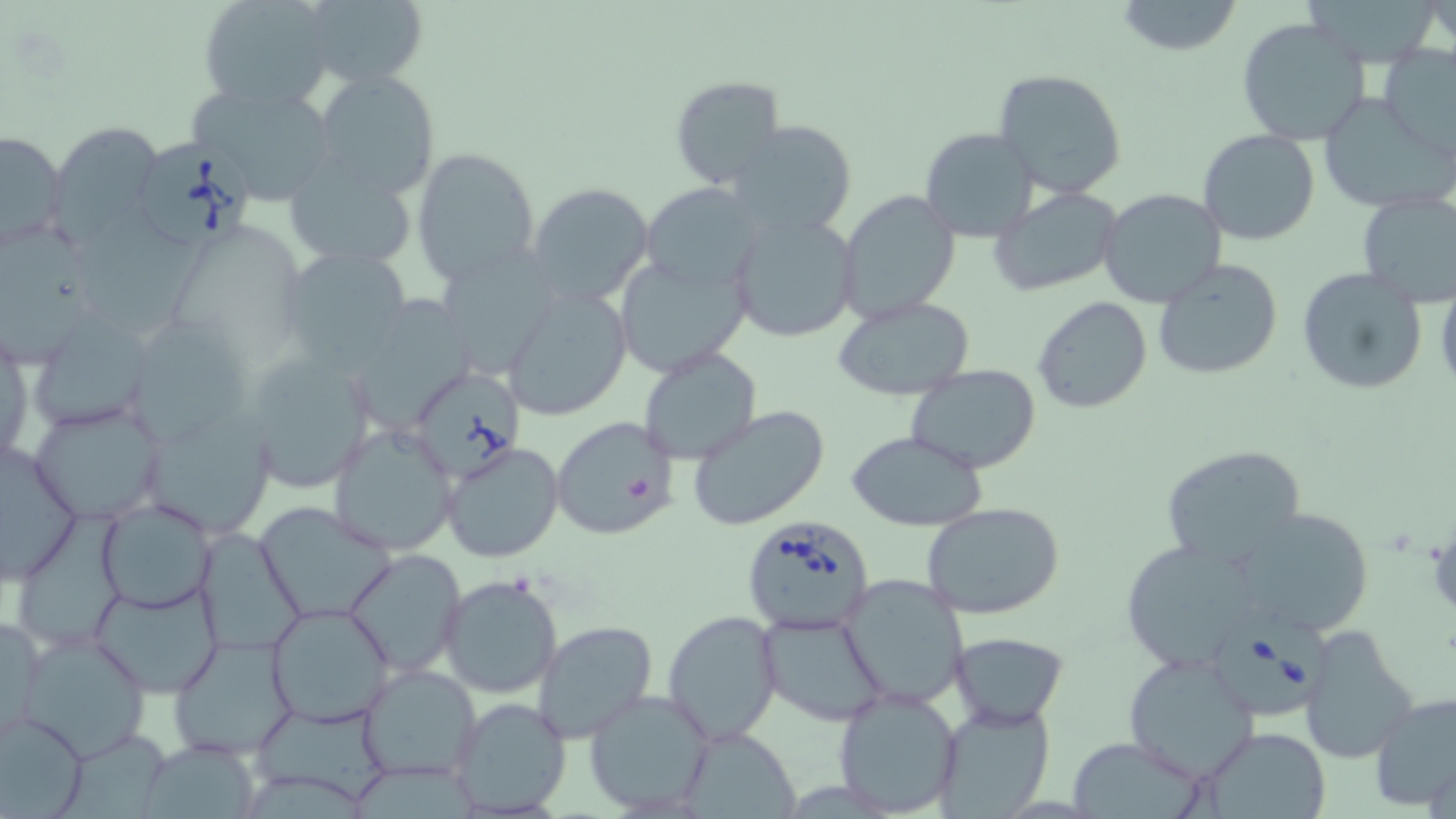
Summary:
  - Coordinate format: approximate bounding boxes as named x1/y1/x2/y2 corners in pixels
  - Uninfected red blood cell locations: (x1=199, y1=0, x2=339, y2=115), (x1=289, y1=0, x2=430, y2=94), (x1=1115, y1=0, x2=1244, y2=57), (x1=1306, y1=1, x2=1440, y2=67), (x1=1236, y1=17, x2=1371, y2=146), (x1=1377, y1=46, x2=1456, y2=157), (x1=992, y1=67, x2=1129, y2=199), (x1=312, y1=69, x2=442, y2=199), (x1=667, y1=75, x2=788, y2=192), (x1=186, y1=79, x2=341, y2=207), (x1=1317, y1=95, x2=1447, y2=214), (x1=726, y1=120, x2=859, y2=237), (x1=49, y1=123, x2=165, y2=244), (x1=919, y1=126, x2=1039, y2=244), (x1=1196, y1=128, x2=1323, y2=246), (x1=0, y1=129, x2=68, y2=250), (x1=411, y1=146, x2=542, y2=287), (x1=282, y1=158, x2=421, y2=269), (x1=528, y1=182, x2=653, y2=307), (x1=640, y1=182, x2=764, y2=294), (x1=990, y1=185, x2=1123, y2=295), (x1=1097, y1=188, x2=1226, y2=307), (x1=836, y1=190, x2=959, y2=322), (x1=1354, y1=191, x2=1456, y2=305), (x1=79, y1=206, x2=209, y2=332), (x1=728, y1=211, x2=860, y2=344), (x1=171, y1=225, x2=294, y2=362), (x1=0, y1=227, x2=108, y2=366), (x1=278, y1=245, x2=415, y2=372), (x1=437, y1=248, x2=562, y2=378), (x1=613, y1=254, x2=750, y2=377), (x1=1154, y1=259, x2=1284, y2=381), (x1=1297, y1=266, x2=1427, y2=396), (x1=502, y1=285, x2=633, y2=420), (x1=361, y1=291, x2=471, y2=431), (x1=833, y1=295, x2=975, y2=400), (x1=1031, y1=295, x2=1153, y2=415), (x1=136, y1=321, x2=251, y2=443), (x1=36, y1=322, x2=146, y2=425), (x1=1, y1=330, x2=32, y2=470), (x1=637, y1=345, x2=763, y2=464), (x1=242, y1=348, x2=379, y2=495), (x1=906, y1=363, x2=1042, y2=474), (x1=28, y1=396, x2=169, y2=525), (x1=685, y1=404, x2=831, y2=532), (x1=550, y1=416, x2=679, y2=540), (x1=146, y1=422, x2=274, y2=535), (x1=328, y1=425, x2=458, y2=556), (x1=846, y1=431, x2=991, y2=530), (x1=0, y1=436, x2=86, y2=587), (x1=440, y1=442, x2=566, y2=565), (x1=1159, y1=443, x2=1307, y2=570), (x1=96, y1=499, x2=216, y2=613), (x1=255, y1=502, x2=397, y2=623), (x1=920, y1=502, x2=1069, y2=621), (x1=1234, y1=505, x2=1375, y2=635), (x1=20, y1=508, x2=126, y2=641), (x1=194, y1=527, x2=304, y2=658), (x1=1116, y1=538, x2=1268, y2=673), (x1=344, y1=549, x2=466, y2=677), (x1=439, y1=575, x2=563, y2=699), (x1=837, y1=575, x2=970, y2=710), (x1=89, y1=578, x2=225, y2=698), (x1=264, y1=603, x2=395, y2=728), (x1=662, y1=610, x2=782, y2=743), (x1=1, y1=611, x2=45, y2=741), (x1=758, y1=612, x2=889, y2=727), (x1=532, y1=620, x2=658, y2=744), (x1=1296, y1=623, x2=1421, y2=763), (x1=14, y1=628, x2=154, y2=761), (x1=950, y1=631, x2=1068, y2=726), (x1=168, y1=634, x2=300, y2=761), (x1=1122, y1=650, x2=1259, y2=782), (x1=356, y1=664, x2=481, y2=783), (x1=830, y1=687, x2=964, y2=816), (x1=583, y1=689, x2=716, y2=817), (x1=1370, y1=692, x2=1456, y2=810), (x1=446, y1=696, x2=573, y2=817), (x1=932, y1=702, x2=1054, y2=817), (x1=252, y1=705, x2=388, y2=802), (x1=0, y1=713, x2=90, y2=816), (x1=677, y1=724, x2=801, y2=818), (x1=1197, y1=727, x2=1334, y2=818), (x1=58, y1=730, x2=174, y2=817), (x1=1065, y1=735, x2=1207, y2=819), (x1=138, y1=739, x2=263, y2=819), (x1=352, y1=763, x2=481, y2=819), (x1=244, y1=767, x2=371, y2=819)
  - Babesia divergens-infected red blood cell locations: (x1=135, y1=140, x2=256, y2=254), (x1=403, y1=362, x2=530, y2=485), (x1=738, y1=514, x2=877, y2=636), (x1=1215, y1=602, x2=1337, y2=721)
  - Slide-level diagnosis: Babesia divergens
  - Modality: optical microscopy
  - Field of view: single
  - Image size: 1456×819 pixels
  - Stain: May-Grünwald-Giemsa
  - Magnification: 1000x
  - Preparation: thin blood film